Classify this cell by malaria status.
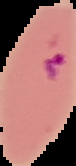
It is parasitized.

Summary:
  - Preparation: thin blood smear
  - Image type: segmented cell region on a black background
  - Image size: 76×166 pixels